Describe the morphology of the red blood cells.
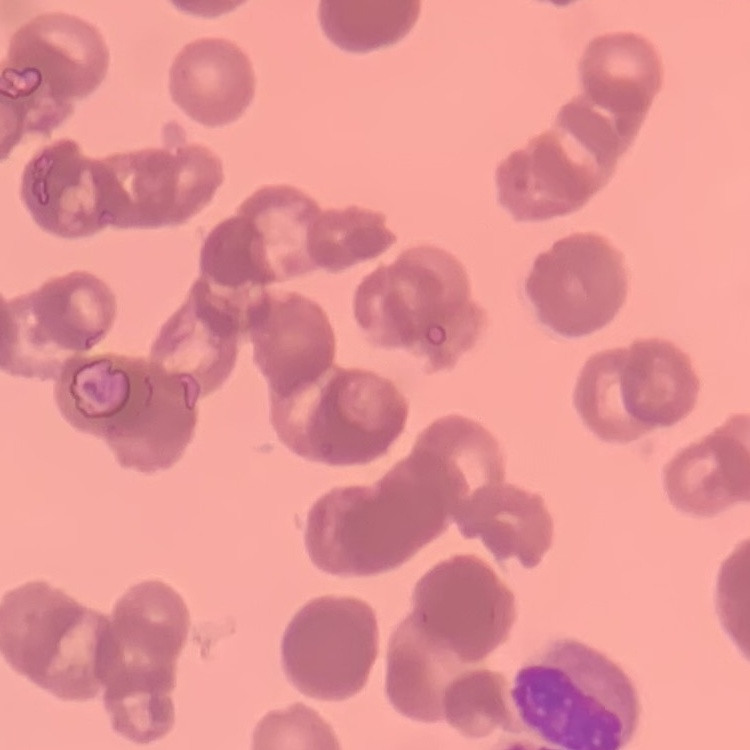

They show rouleaux formation.

Thin blood smear. Square crop of a larger photomicrograph. Stained with either Field's or Giemsa.